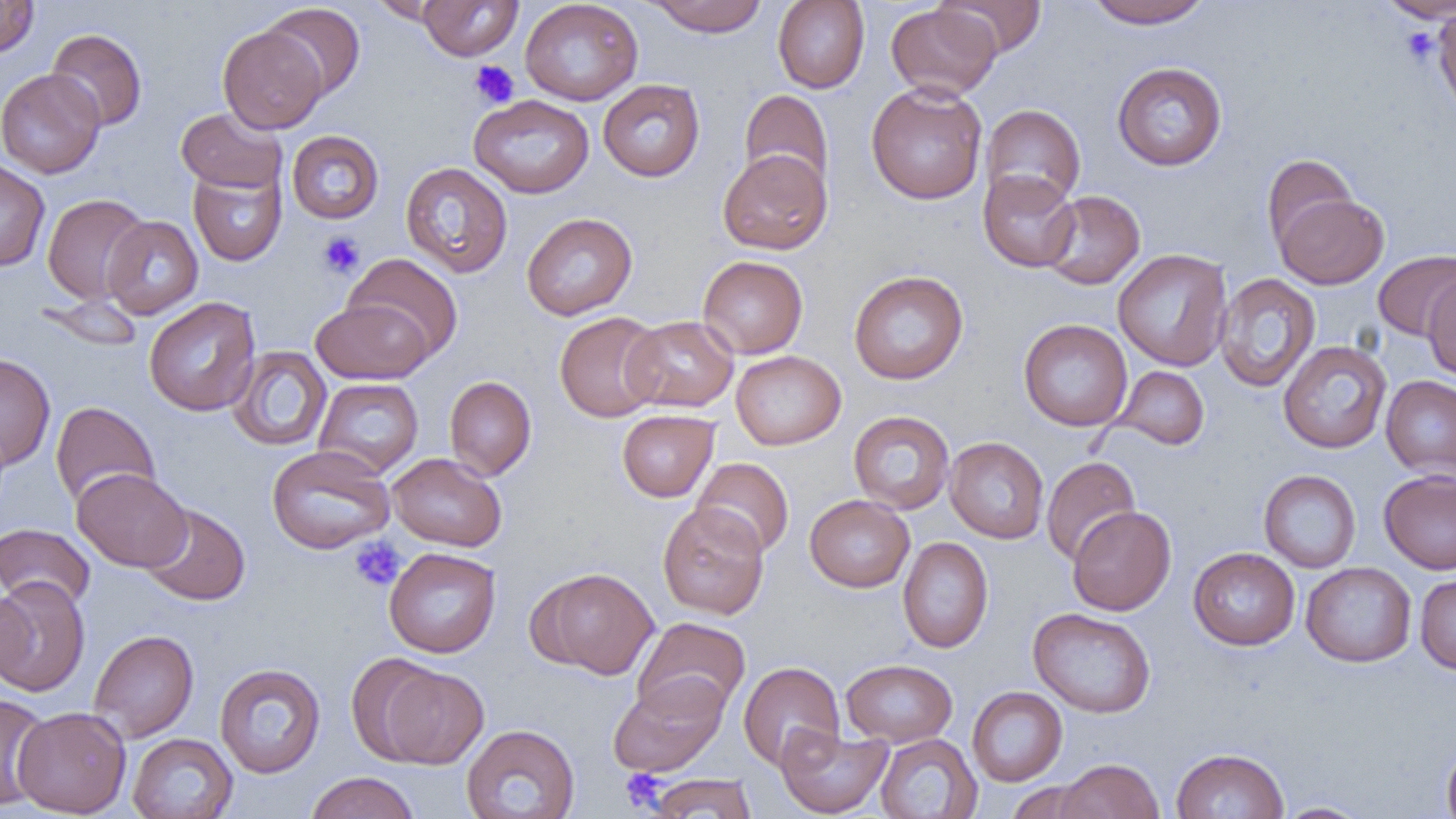

slide_level_diagnosis: no evidence of blood parasites
image_size: 1456×819 pixels
modality: optical microscopy
uninfected_red_blood_cell_locations: 'approximate bounding boxes as (x1, y1, x2, y2) in pixels: (0, 0, 39, 59), (371, 0, 458, 25), (418, 0, 522, 61), (519, 0, 643, 106), (934, 0, 1047, 58), (1085, 0, 1213, 29), (1377, 0, 1456, 22), (644, 1, 769, 36), (773, 1, 870, 93), (261, 3, 366, 100), (885, 3, 1001, 100), (1433, 4, 1456, 118), (1422, 19, 1454, 86), (218, 25, 327, 134), (46, 29, 147, 131), (1112, 62, 1227, 171), (0, 68, 106, 178), (598, 79, 705, 182), (866, 82, 987, 205), (739, 89, 834, 191), (469, 94, 594, 198), (981, 104, 1086, 209), (176, 107, 287, 194), (286, 130, 384, 224), (718, 149, 832, 254), (1261, 154, 1359, 254), (0, 158, 50, 273), (401, 162, 513, 277), (188, 164, 287, 266), (979, 170, 1080, 272), (1040, 190, 1145, 289), (42, 193, 151, 305), (1274, 193, 1389, 289), (522, 212, 637, 320), (102, 216, 204, 319), (1373, 248, 1456, 342), (1113, 249, 1232, 371), (344, 253, 463, 361), (697, 255, 808, 359), (848, 270, 968, 385), (1422, 272, 1456, 381), (1214, 273, 1321, 392), (35, 295, 145, 352), (144, 297, 261, 416), (311, 298, 433, 384), (554, 312, 666, 422), (623, 315, 738, 413), (1018, 318, 1133, 431), (1278, 341, 1392, 454), (227, 346, 332, 451), (731, 350, 846, 450), (0, 353, 56, 470), (1112, 365, 1210, 450), (1381, 374, 1456, 481), (444, 376, 537, 481), (313, 378, 424, 478), (50, 401, 160, 508), (616, 410, 719, 502), (848, 411, 956, 514), (945, 437, 1049, 543), (267, 445, 395, 554), (387, 453, 507, 551), (1041, 456, 1141, 566), (691, 457, 795, 558), (72, 468, 192, 572), (1378, 469, 1456, 574), (1259, 470, 1361, 572), (804, 494, 915, 593), (657, 502, 769, 619), (140, 503, 250, 606), (1067, 506, 1176, 616), (0, 523, 95, 610), (898, 537, 994, 653), (384, 547, 501, 657), (1188, 547, 1300, 650), (1301, 562, 1417, 667), (534, 567, 659, 679), (1415, 574, 1456, 674), (0, 575, 90, 698), (0, 586, 31, 688), (1028, 607, 1156, 718), (632, 617, 751, 719), (88, 629, 199, 743), (346, 653, 447, 765), (841, 659, 957, 747), (738, 661, 844, 770), (214, 663, 325, 778), (377, 665, 488, 769), (608, 674, 729, 776), (967, 686, 1067, 786), (0, 693, 50, 811), (12, 706, 131, 817), (775, 723, 892, 818), (461, 724, 580, 819), (128, 732, 238, 819), (874, 733, 982, 818), (1442, 740, 1456, 819), (1170, 747, 1289, 819), (1054, 758, 1164, 819), (304, 772, 420, 819), (647, 774, 757, 818), (1005, 781, 1099, 818), (1274, 801, 1376, 818)'
platelet_locations: 'approximate bounding boxes as (x1, y1, x2, y2) in pixels: (1402, 28, 1438, 66), (470, 60, 520, 109), (317, 232, 365, 279), (350, 537, 405, 591), (620, 769, 666, 811)'
preparation: thin blood smear
magnification: 1000x
field_of_view: one of a larger specimen